Classify this cell by malaria status.
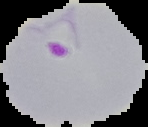
Parasitized.

From a thin blood film. Segmented cell region on a black background. Image is 148×127 pixels.